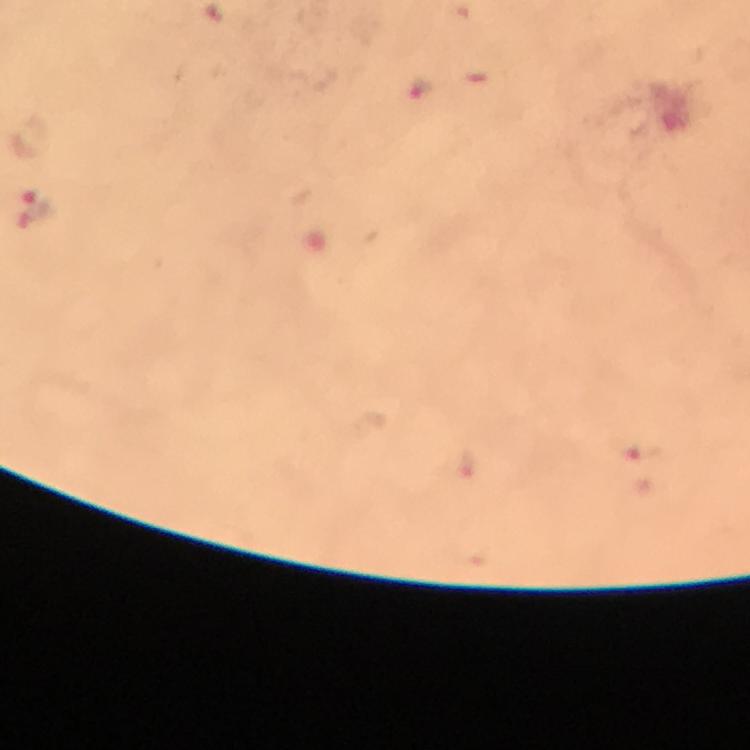

{
  "stain": "Giemsa",
  "magnification": "100x",
  "cropped_from": "a single field of view",
  "preparation": "thick smear",
  "immersion_oil": "used",
  "context": "from a malaria diagnostic workup",
  "capture": "smartphone mounted on the microscope",
  "image_size": "750×750 pixels",
  "plasmodium_parasite_locations": "approximate centers as [x, y] in pixels: [421, 89], [39, 211], [641, 456]"
}